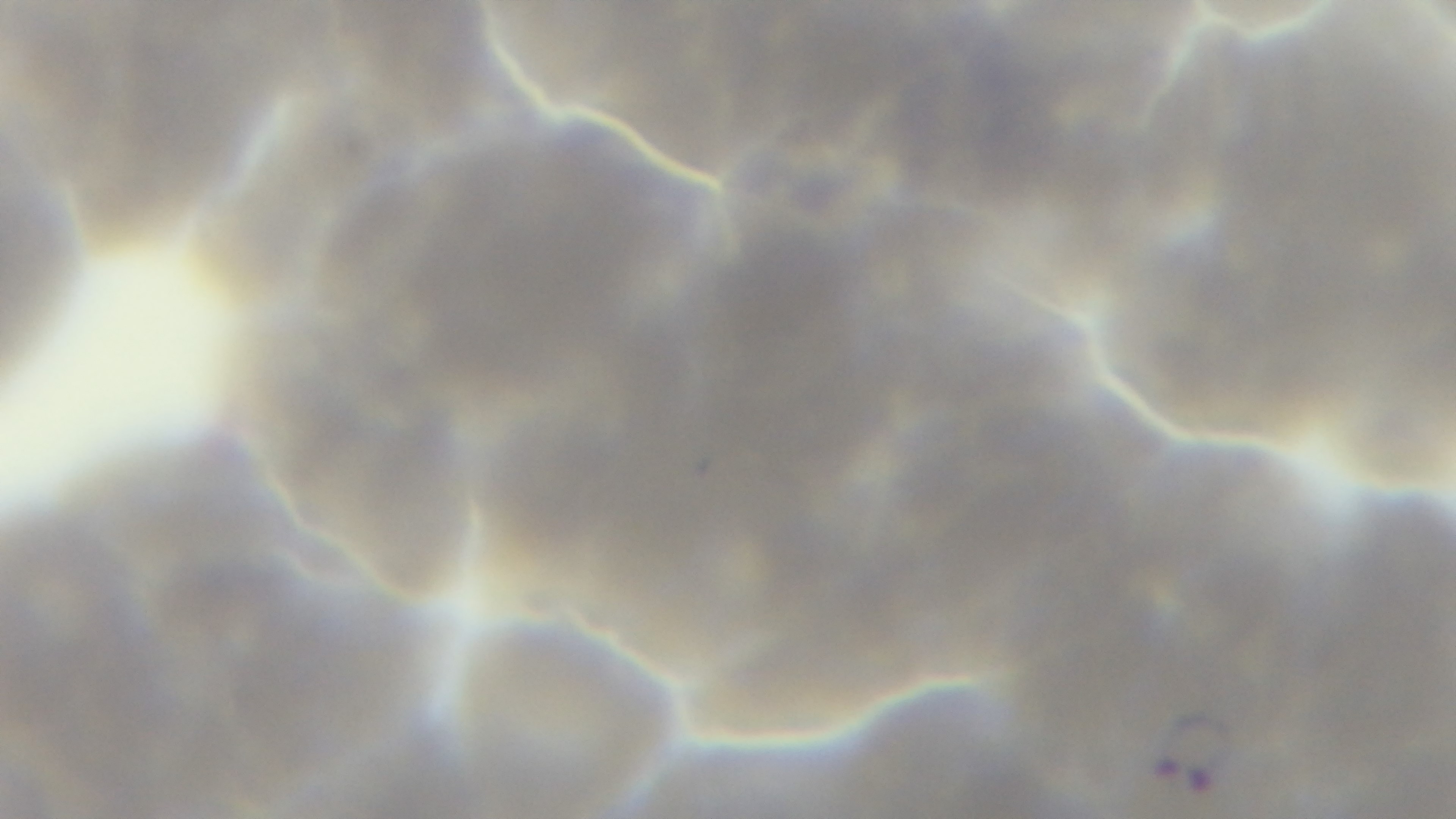
Summary:
  - Modality: light microscopy
  - Capture: mounted 4K digital camera
  - Stain: Giemsa
  - Field of view: one from the slide
  - Objective: 100x oil immersion
  - Malaria status: infected
  - Preparation: thin blood film